Report the malaria status of this cell.
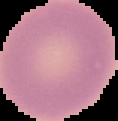
It is uninfected.

image_type: segmented cell region with the area outside set to black
preparation: thin blood film
image_size: 118×121 pixels